Classify this cell by malaria status.
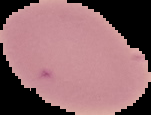

It is uninfected.

Summary:
  - Preparation: thin blood smear
  - Image size: 151×115 pixels
  - Image type: segmented cell region on a black background